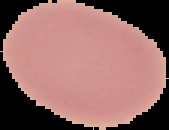

Image is 169×130 pixels. The area outside the segmented cell region is set to black. Result: negative for malaria parasites. From a thin blood film.